Name the parasite shown.
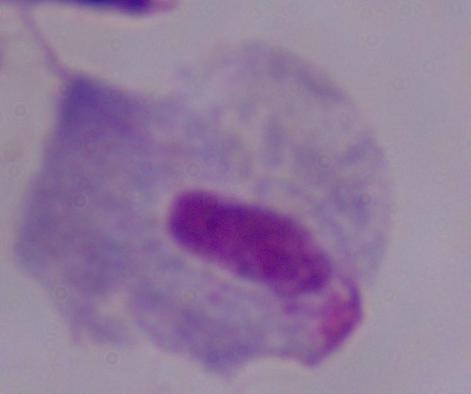
This is a trichomonad.

Summary:
  - Modality: micrograph
  - Magnification: 1000x